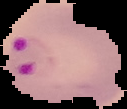

image size = 127×109 pixels
image type = segmented cell region with the area outside set to black
malaria status = parasitized
preparation = thin blood film